Assess this cell for malaria.
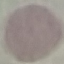

It is uninfected.

preparation = thin blood film
capture = smartphone through the microscope eyepiece
stain = Giemsa
image type = automatically extracted cell patch, resized to 64 × 64 pixels